Evaluate for malaria.
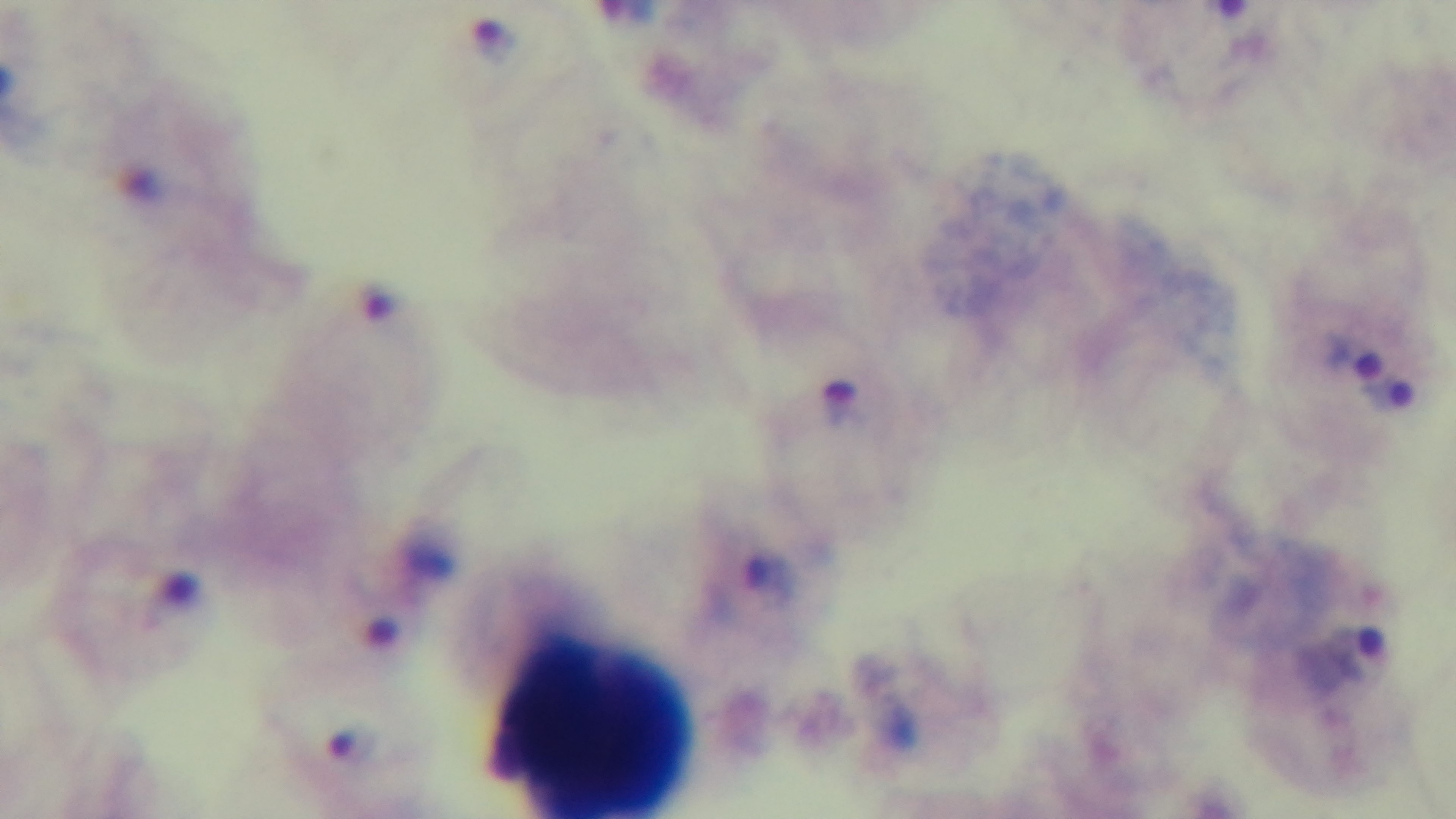

It is infected.

Photomicrograph. Preparation: thick blood film. Captured with a mounted 4K digital camera. One field from the slide. Giemsa-stained. Oil-immersion objective, 100x.